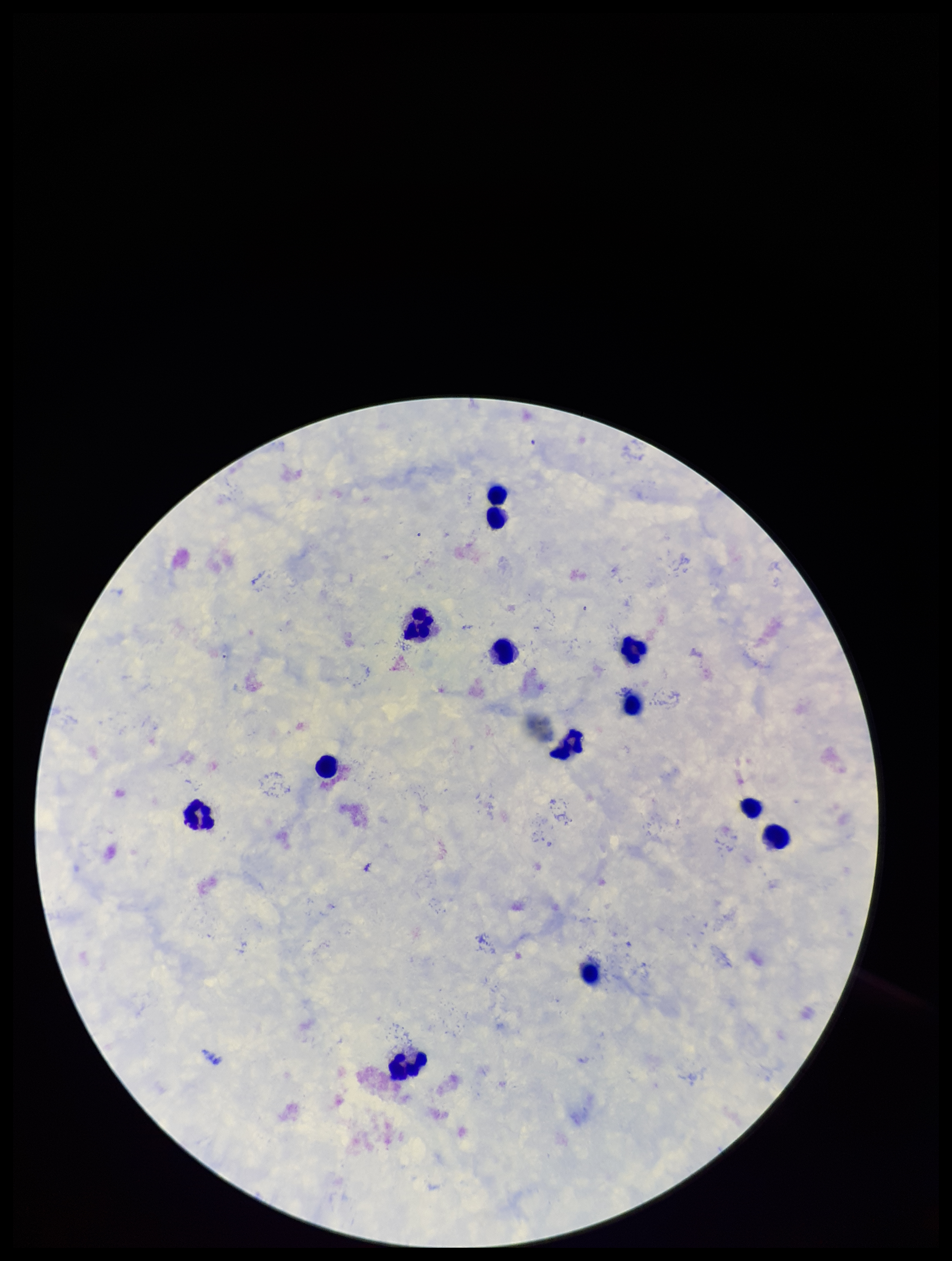

Summary:
  - Leukocyte count: 13
  - Preparation: thick
  - Plasmodium parasites: none detected
  - Parasite count: 0
  - Capture: smartphone photograph through the microscope eyepiece
  - Field of view: one from this slide
  - Stain: Giemsa
  - Patient malaria status: negative
  - Image size: 952×1261 pixels